Outline each uninfected red blood cell.
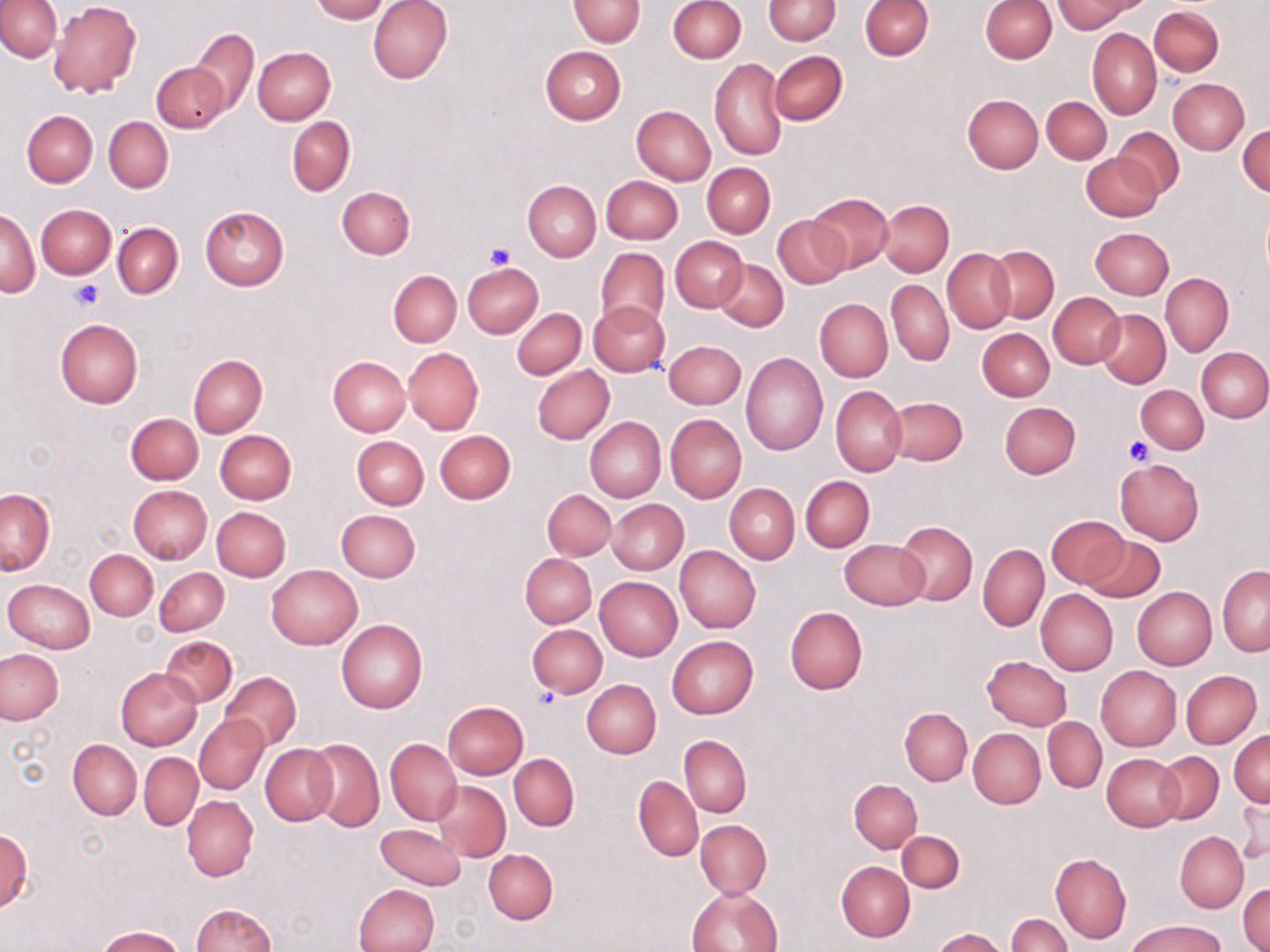

Approximate bounding boxes as [x1, y1, x2, y2] in pixels.
Uninfected red blood cells: [310, 0, 390, 23], [369, 0, 453, 85], [568, 0, 645, 46], [668, 0, 746, 63], [764, 0, 840, 44], [860, 0, 933, 60], [980, 0, 1057, 63], [1053, 0, 1139, 33], [0, 1, 61, 61], [50, 3, 142, 98], [1149, 6, 1224, 77], [189, 28, 259, 116], [1087, 28, 1160, 119], [540, 45, 626, 124], [252, 46, 335, 125], [769, 51, 847, 126], [709, 58, 788, 160], [151, 62, 229, 133], [1168, 79, 1249, 154], [962, 94, 1043, 174], [1042, 96, 1111, 164], [632, 106, 715, 185], [21, 111, 97, 187], [104, 117, 173, 192], [287, 117, 355, 196], [1237, 124, 1270, 197], [1113, 128, 1185, 198], [1083, 153, 1160, 223], [702, 162, 775, 238], [601, 175, 682, 244], [522, 181, 601, 261], [337, 186, 415, 259], [807, 192, 894, 271], [877, 200, 954, 277], [36, 205, 115, 279], [199, 206, 290, 290], [1, 208, 39, 298], [774, 214, 852, 288], [112, 222, 183, 299], [1089, 228, 1173, 299], [672, 237, 747, 312], [987, 245, 1059, 321], [595, 247, 669, 330], [942, 248, 1015, 333], [715, 260, 789, 331], [462, 262, 544, 338], [388, 270, 461, 346], [1160, 273, 1233, 355], [887, 279, 953, 366], [1048, 292, 1124, 368], [815, 299, 892, 382], [589, 301, 670, 377], [512, 308, 586, 380], [1097, 310, 1170, 387], [55, 317, 143, 407], [977, 328, 1054, 401], [663, 341, 746, 409], [402, 347, 483, 435], [1196, 347, 1270, 422], [740, 352, 827, 455], [188, 354, 267, 438], [329, 356, 410, 436], [532, 365, 614, 444], [1136, 384, 1209, 454], [831, 385, 907, 475], [886, 395, 968, 466], [999, 402, 1081, 478], [125, 413, 203, 485], [666, 414, 746, 503], [584, 417, 665, 502], [214, 430, 297, 504], [434, 430, 516, 504], [352, 436, 427, 509], [1115, 459, 1205, 545], [800, 475, 874, 551], [725, 483, 799, 564], [128, 485, 212, 564], [1, 488, 55, 575], [542, 489, 615, 560], [606, 499, 687, 573], [211, 507, 290, 582], [336, 509, 420, 583], [1046, 514, 1127, 589], [895, 521, 977, 606], [1081, 534, 1164, 602], [839, 539, 929, 609], [978, 543, 1049, 632], [674, 545, 760, 633], [86, 549, 158, 620], [520, 554, 597, 627], [267, 565, 363, 649], [1217, 566, 1269, 655], [155, 567, 229, 635], [595, 576, 682, 660], [4, 579, 95, 654], [1132, 587, 1217, 669], [1036, 589, 1118, 675], [785, 606, 867, 694], [336, 619, 427, 713], [527, 624, 606, 697], [160, 635, 237, 706], [666, 635, 758, 720], [0, 650, 65, 724], [982, 656, 1072, 730], [1096, 666, 1181, 751], [116, 667, 202, 751], [1181, 670, 1260, 748], [220, 671, 301, 751], [582, 679, 661, 758], [442, 700, 528, 779], [900, 707, 972, 786], [195, 716, 269, 793], [1043, 717, 1107, 793], [967, 728, 1045, 809], [1229, 730, 1269, 808], [680, 735, 751, 817], [306, 737, 385, 831], [68, 739, 142, 820], [385, 739, 461, 825], [260, 744, 338, 825], [138, 752, 202, 830], [1101, 752, 1185, 831], [1155, 752, 1223, 825], [509, 753, 579, 831], [633, 776, 703, 862], [848, 779, 922, 852], [433, 781, 511, 861], [1234, 792, 1269, 864], [182, 795, 257, 881], [696, 820, 771, 899], [375, 822, 465, 890], [0, 828, 32, 911], [1175, 830, 1248, 912], [897, 831, 965, 893], [484, 848, 557, 923], [1050, 853, 1131, 944], [837, 861, 915, 941], [354, 883, 440, 952], [1239, 884, 1269, 951], [687, 886, 781, 952], [189, 903, 275, 952], [1006, 914, 1071, 951], [1127, 919, 1225, 952], [93, 926, 184, 952], [934, 928, 1009, 952].

Summary:
  - Platelet locations: [487, 243, 515, 270], [70, 281, 103, 310], [1124, 436, 1155, 464], [530, 692, 559, 712]
  - Slide-level diagnosis: negative for blood parasites
  - Preparation: thin blood smear
  - Field of view: one of a larger specimen
  - Image size: 1270×952 pixels
  - Magnification: 1000x
  - Modality: light microscopy
  - Stain: May-Grünwald-Giemsa